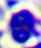

{
  "modality": "photomicrograph",
  "magnification": "400x",
  "identification": "leukocyte"
}